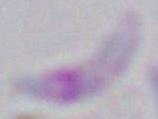
identification = Toxoplasma gondii
modality = photomicrograph
magnification = 1000x